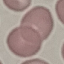
Result: no malaria parasites detected. Acquired by smartphone through the microscope eyepiece. Cell patch, automatically extracted from a larger field of view and resized to 64 × 64 pixels. Giemsa-stained preparation. Thin blood film.